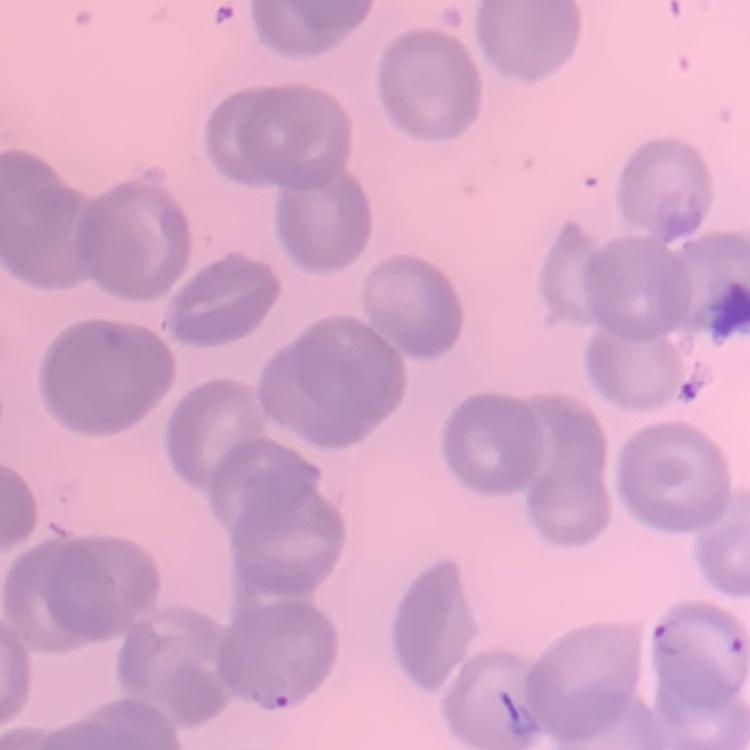 The erythrocytes exhibit no rouleaux formation. Thin blood film. Square crop of a larger photomicrograph. Stained with either Field's or Giemsa.